Identify the parasite.
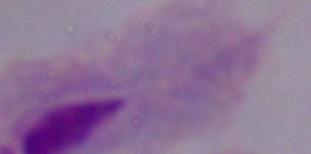

A trichomonad.

1000x magnification. Photomicrograph.